Assess this cell for malaria.
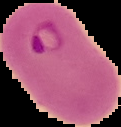

Parasitized.

From a thin blood smear. Image is 121×127 pixels. Cell region segmented out of the field of view; the surrounding area is masked to black.